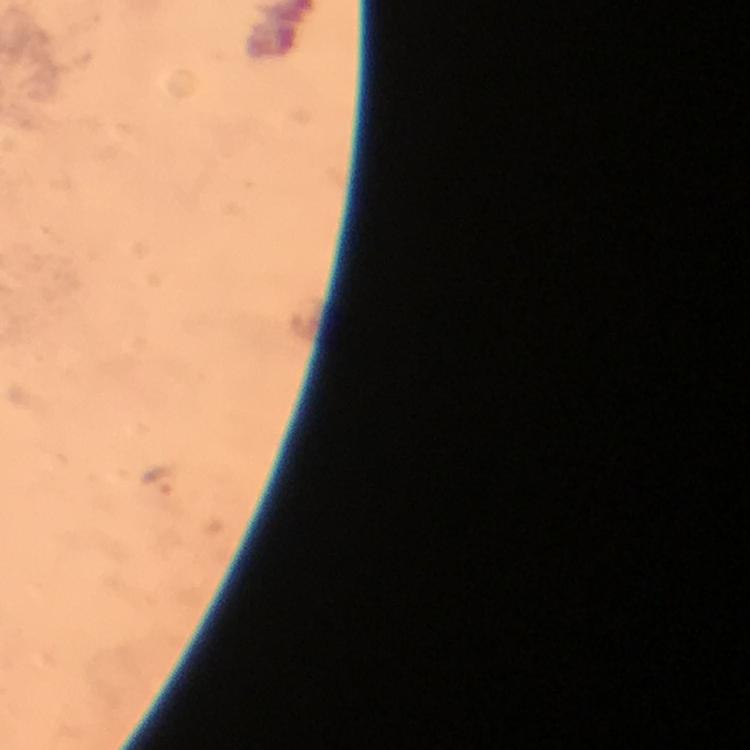
Approximate object centers, in pixels from the top-left corner.
Summary:
  - Plasmodium parasite locations: (x=160, y=480)
  - Image size: 750×750 pixels
  - Immersion oil: applied
  - Capture: smartphone camera through the microscope
  - Stain: Giemsa
  - Cropped from: one field of view
  - Context: from a diagnostic examination for malaria
  - Preparation: thick blood film
  - Magnification: 100x